Give the extent of all Plasmodium vivax-infected red blood cells.
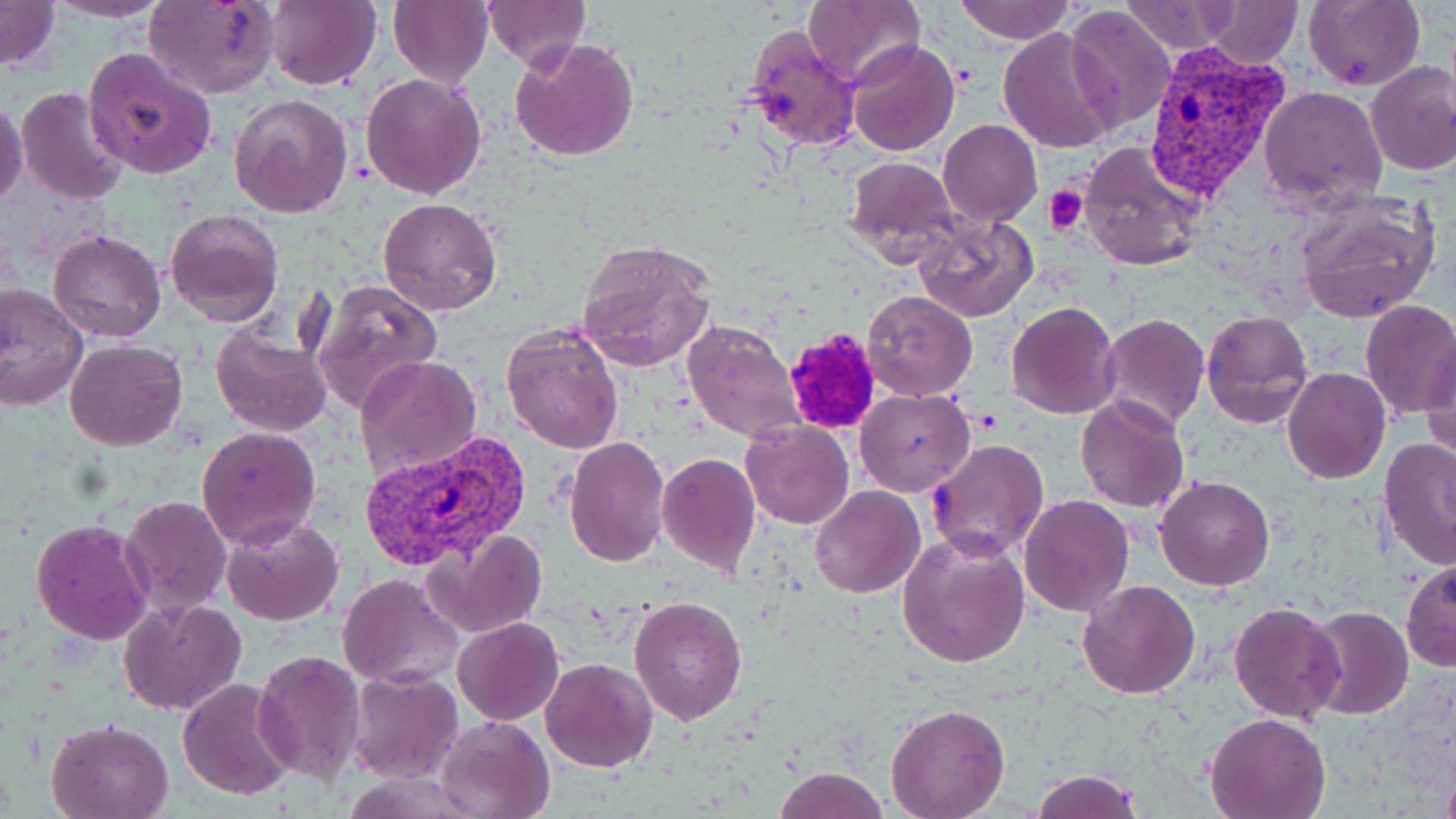
Approximate bounding boxes as [x1, y1, x2, y2] in pixels.
Plasmodium vivax-infected red blood cells: [1145, 43, 1293, 202], [355, 431, 530, 572].

Platelet locations: [1046, 184, 1090, 236], [783, 329, 883, 433]. Uninfected red blood cell locations: [0, 0, 59, 73], [45, 0, 171, 22], [145, 0, 279, 99], [264, 0, 381, 91], [389, 0, 493, 89], [481, 0, 589, 67], [802, 0, 925, 92], [953, 0, 1076, 44], [1199, 0, 1302, 66], [1303, 0, 1425, 89], [1118, 1, 1243, 54], [1064, 6, 1177, 132], [739, 23, 862, 152], [999, 28, 1119, 152], [509, 36, 640, 160], [848, 39, 959, 156], [83, 46, 218, 179], [1365, 60, 1456, 177], [360, 72, 487, 199], [17, 86, 131, 205], [1258, 86, 1386, 209], [229, 93, 355, 217], [1, 95, 26, 206], [939, 119, 1042, 226], [1078, 140, 1209, 271], [844, 158, 959, 263], [1294, 194, 1442, 323], [380, 198, 502, 315], [165, 208, 285, 328], [912, 213, 1039, 323], [48, 228, 166, 342], [574, 240, 716, 373], [310, 280, 443, 414], [0, 285, 90, 411], [863, 290, 977, 399], [1006, 301, 1121, 419], [1358, 301, 1456, 420], [1200, 310, 1314, 428], [1099, 314, 1210, 430], [681, 318, 806, 444], [501, 324, 625, 453], [210, 326, 334, 437], [66, 338, 186, 451], [1420, 346, 1455, 463], [355, 354, 482, 480], [1283, 366, 1390, 484], [856, 390, 974, 496], [1076, 395, 1190, 513], [740, 420, 853, 530], [197, 426, 322, 551], [563, 435, 671, 567], [929, 438, 1050, 561], [1379, 439, 1456, 570], [656, 453, 760, 576], [1154, 475, 1275, 590], [811, 486, 925, 599], [1019, 494, 1134, 617], [119, 497, 233, 618], [222, 512, 345, 625], [31, 517, 155, 646], [426, 527, 548, 638], [897, 530, 1031, 669], [1401, 558, 1456, 672], [338, 574, 465, 689], [1077, 580, 1201, 699], [627, 594, 747, 725], [120, 598, 245, 716], [1227, 600, 1345, 722], [1302, 605, 1414, 721], [452, 616, 563, 724], [251, 649, 367, 787], [539, 657, 658, 772], [348, 668, 462, 783], [177, 678, 296, 801], [886, 703, 1009, 819], [1203, 713, 1330, 819], [436, 715, 556, 819], [47, 719, 175, 819], [773, 766, 888, 819], [1030, 771, 1146, 819]. Slide-level diagnosis: Plasmodium vivax. Optical microscopy. Image is 1456×819 pixels. Captured at 1000x magnification. May-Grünwald-Giemsa-stained preparation. Thin blood film. One field of a larger specimen.